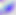
modality = photomicrograph
magnification = 400x
identification = Toxoplasma gondii